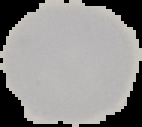
Summary:
  - Malaria status: uninfected
  - Image size: 142×127 pixels
  - Preparation: thin blood smear
  - Image type: segmented cell region on a black background